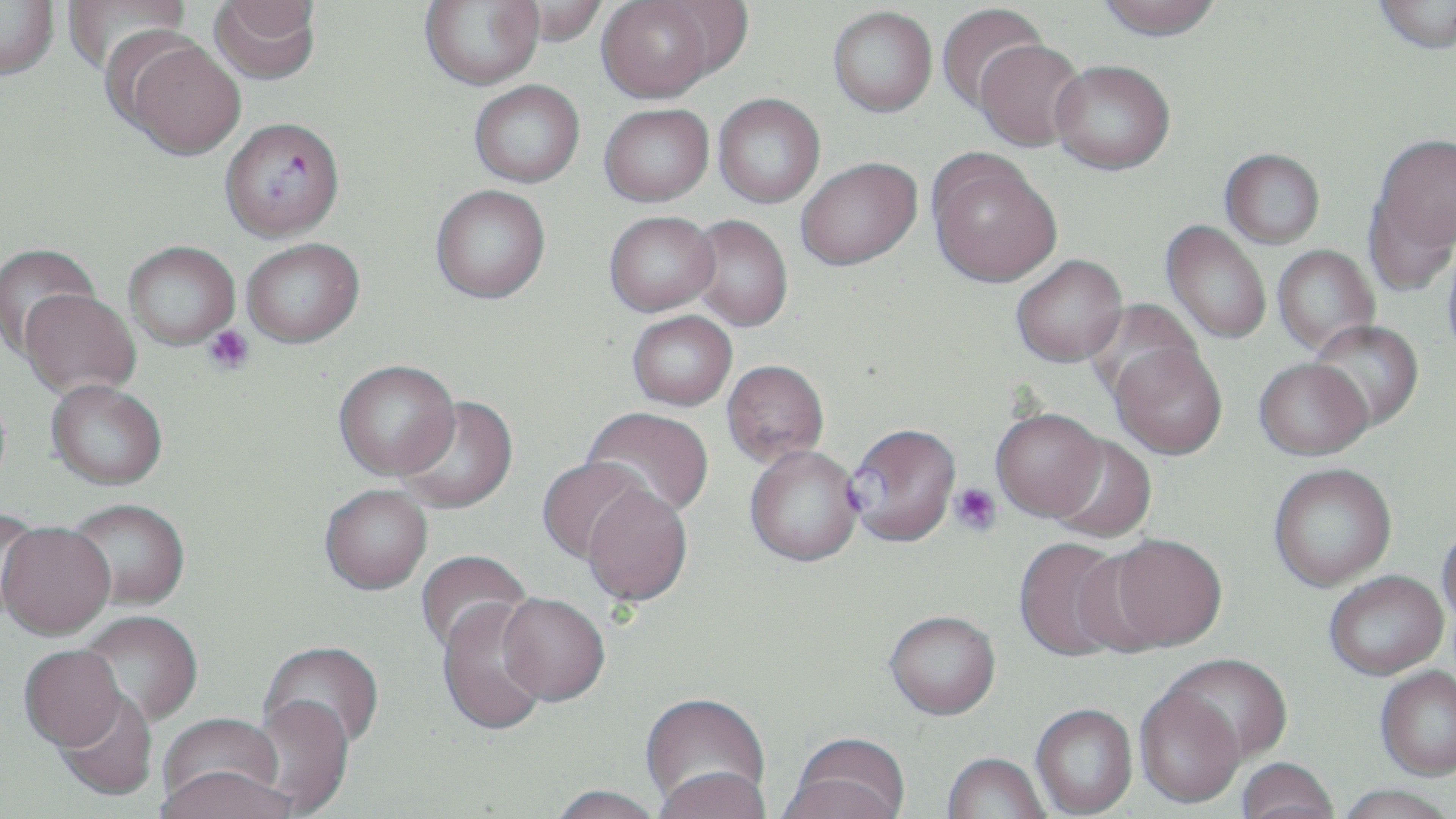
Summary:
  - Coordinate format: approximate bounding boxes as [x1, y1, x2, y2] in pixels
  - Uninfected red blood cell locations: [0, 0, 59, 80], [61, 0, 191, 76], [208, 0, 321, 84], [419, 0, 543, 90], [501, 0, 608, 48], [1372, 0, 1456, 54], [597, 1, 716, 102], [652, 1, 754, 82], [1095, 1, 1224, 40], [936, 3, 1048, 114], [828, 6, 937, 117], [123, 38, 245, 159], [974, 39, 1087, 151], [1050, 59, 1175, 175], [469, 80, 585, 187], [713, 93, 825, 207], [599, 103, 714, 206], [1372, 132, 1456, 260], [926, 149, 1061, 288], [1220, 149, 1325, 248], [796, 157, 921, 270], [430, 184, 550, 303], [1364, 186, 1455, 298], [604, 211, 720, 315], [686, 215, 793, 331], [1161, 220, 1271, 344], [241, 238, 364, 347], [123, 240, 240, 349], [0, 243, 100, 358], [1272, 245, 1379, 356], [1010, 254, 1127, 367], [19, 289, 140, 398], [1083, 299, 1203, 407], [627, 310, 737, 410], [1307, 319, 1424, 431], [1110, 341, 1228, 460], [1254, 357, 1373, 460], [334, 359, 459, 479], [721, 360, 829, 468], [45, 382, 168, 493], [396, 396, 518, 515], [582, 407, 714, 520], [990, 408, 1107, 521], [1046, 435, 1156, 543], [744, 445, 863, 568], [537, 456, 649, 564], [1268, 463, 1397, 591], [582, 484, 692, 606], [319, 486, 433, 597], [66, 501, 189, 614], [0, 508, 44, 624], [1437, 521, 1456, 628], [0, 526, 115, 644], [1102, 533, 1228, 652], [1014, 536, 1132, 662], [415, 550, 531, 661], [1324, 570, 1448, 680], [496, 597, 609, 710], [436, 601, 550, 739], [78, 613, 203, 730], [884, 613, 1000, 723], [259, 643, 385, 755], [18, 648, 127, 755], [1163, 654, 1293, 766], [1376, 667, 1456, 781], [1134, 687, 1246, 810], [53, 690, 157, 803], [641, 695, 770, 814], [250, 699, 353, 814], [1031, 706, 1137, 818], [157, 715, 286, 814], [784, 736, 911, 819], [942, 755, 1050, 819], [1236, 759, 1340, 819], [157, 770, 293, 819], [653, 770, 772, 819], [1332, 786, 1456, 819], [546, 788, 665, 819]
  - Platelet locations: [202, 324, 255, 375], [949, 483, 1001, 536]
  - Plasmodium falciparum-infected red blood cell locations: [220, 117, 344, 242], [846, 422, 962, 548]
  - Slide-level diagnosis: Plasmodium falciparum
  - Preparation: thin blood film
  - Field of view: single
  - Stain: May-Grünwald-Giemsa
  - Image size: 1456×819 pixels
  - Magnification: 1000x
  - Modality: optical microscopy